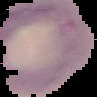

Summary:
  - Preparation: thin blood film
  - Malaria status: parasitized
  - Image size: 97×97 pixels
  - Image type: segmented cell region with the area outside set to black